Give the extent of all Plasmodium malariae-infected red blood cells.
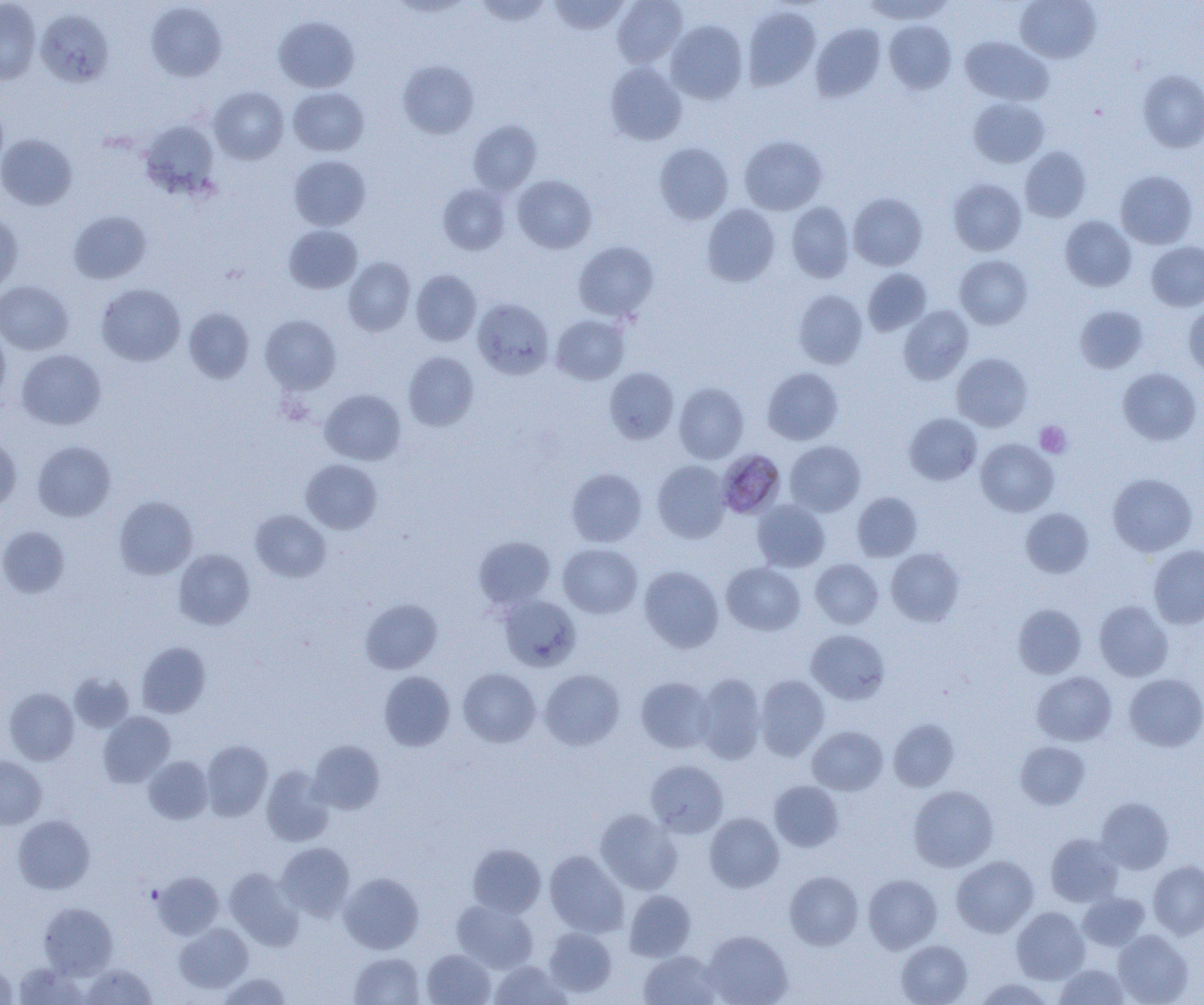
Approximate bounding boxes as (x1,y1)-(x2,y2) corner pairs in pixels.
Plasmodium malariae-infected red blood cells: (720,450)-(789,520).

Platelet locations: (1035,421)-(1072,458), (146,886)-(163,903). Uninfected red blood cell locations: (0,0)-(41,84), (475,0)-(552,26), (548,0)-(630,35), (612,0)-(688,67), (862,0)-(954,23), (1015,0)-(1101,63), (389,1)-(473,18), (145,2)-(227,81), (742,6)-(820,91), (36,9)-(114,87), (274,16)-(360,92), (666,20)-(748,104), (884,20)-(956,93), (811,22)-(886,101), (960,37)-(1053,106), (398,60)-(479,138), (605,62)-(687,145), (1138,70)-(1204,152), (209,87)-(289,164), (288,87)-(369,156), (968,98)-(1050,168), (139,119)-(220,199), (468,120)-(542,195), (0,134)-(78,210), (739,135)-(827,215), (654,143)-(733,224), (1020,147)-(1091,221), (289,155)-(370,231), (1115,170)-(1197,249), (512,174)-(597,253), (948,178)-(1026,255), (438,183)-(511,255), (848,193)-(927,270), (786,202)-(855,282), (702,204)-(780,286), (69,210)-(152,284), (0,211)-(23,294), (1060,216)-(1136,291), (284,224)-(363,294), (573,241)-(659,321), (1146,242)-(1204,311), (955,255)-(1032,329), (343,257)-(415,336), (410,269)-(481,346), (863,269)-(932,336), (0,280)-(73,355), (96,283)-(185,366), (793,290)-(867,368), (472,299)-(554,379), (1183,304)-(1204,378), (898,305)-(974,384), (1074,305)-(1148,373), (183,307)-(254,384), (550,314)-(629,385), (260,315)-(341,394), (0,324)-(11,407), (17,349)-(106,430), (403,351)-(479,431), (952,353)-(1032,431), (604,367)-(679,444), (762,367)-(843,445), (1118,367)-(1201,445), (674,382)-(749,464), (320,389)-(406,465), (904,413)-(982,485), (0,435)-(21,513), (976,438)-(1058,517), (32,441)-(115,522), (785,441)-(866,516), (301,459)-(382,534), (652,460)-(731,542), (566,468)-(646,547), (1108,473)-(1197,556), (852,492)-(922,561), (114,496)-(198,579), (752,500)-(830,572), (1020,507)-(1093,578), (250,510)-(331,581), (0,526)-(70,598), (474,536)-(555,609), (558,543)-(642,618), (1149,545)-(1204,629), (886,547)-(964,626), (174,549)-(255,630), (810,558)-(883,629), (722,562)-(805,636), (639,565)-(723,652), (499,594)-(581,671), (360,598)-(442,673), (1093,600)-(1173,681), (1013,603)-(1087,678), (806,629)-(890,704), (136,642)-(210,718), (458,668)-(541,747), (539,669)-(625,751), (379,671)-(455,751), (1032,671)-(1117,746), (69,672)-(134,732), (694,673)-(766,764), (1124,673)-(1204,751), (755,675)-(829,760), (636,677)-(715,753), (3,687)-(79,765), (98,712)-(175,787), (889,718)-(959,792), (807,726)-(888,795), (201,739)-(273,821), (309,740)-(385,814), (1015,741)-(1090,809), (0,756)-(46,829), (143,756)-(213,824), (646,759)-(728,838), (261,766)-(334,846), (769,781)-(844,852), (908,785)-(998,872), (1095,797)-(1174,874), (594,809)-(682,895), (705,812)-(784,893), (13,815)-(94,893), (1046,833)-(1122,907), (277,842)-(354,919), (468,843)-(546,917), (545,850)-(628,937), (952,855)-(1038,937), (1148,860)-(1204,939), (224,867)-(304,949), (153,871)-(224,939), (785,871)-(863,949), (339,872)-(423,953), (863,875)-(942,953), (624,890)-(696,961), (1078,892)-(1150,950), (452,900)-(538,973), (39,903)-(117,977), (1011,907)-(1089,984), (175,923)-(253,993), (544,927)-(617,997), (703,930)-(793,1005), (1113,930)-(1193,1005), (896,940)-(972,1005), (422,949)-(495,1005), (639,951)-(723,1005), (349,952)-(425,1005), (489,961)-(571,1005), (0,962)-(17,1004), (13,962)-(87,1004), (81,963)-(156,1004), (1053,964)-(1130,1005), (217,972)-(293,1004), (973,978)-(1056,1005). Slide-level diagnosis: Plasmodium malariae. Single field of view. Captured at 1000x magnification. Image is 1204×1005 pixels. Thin blood smear. Light microscopy.